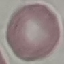

malaria status = uninfected
preparation = thin smear
stain = Giemsa
capture = smartphone camera at the microscope eyepiece
image type = cell patch, automatically extracted from a larger field of view and resized to 64 × 64 pixels